Classify this cell by malaria status.
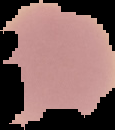
Uninfected.

Summary:
  - Image size: 115×130 pixels
  - Image type: cell region segmented out of the field of view; surrounding area masked to black
  - Preparation: thin blood smear